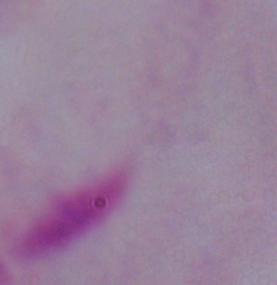

Summary:
  - Magnification: 1000x
  - Modality: micrograph
  - Identification: trichomonad